Assess this cell for malaria.
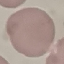

It is uninfected.

stain = Giemsa
preparation = thin smear
image type = cell patch, automatically extracted from a larger field of view and resized to 64 × 64 pixels
capture = smartphone camera at the microscope eyepiece